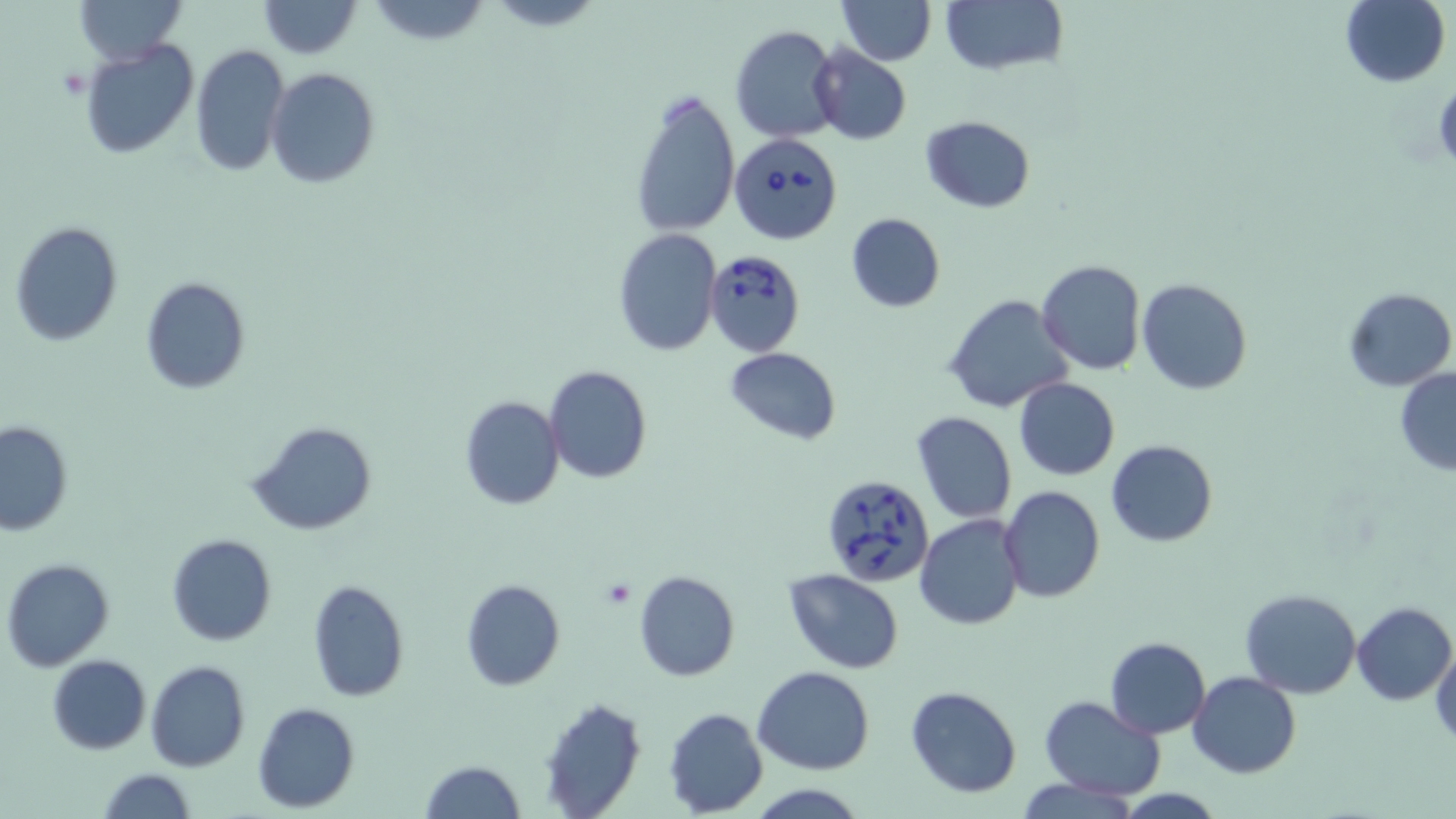 Approximate bounding boxes as named x1/y1/x2/y2 corners in pixels. Babesia divergens-infected red blood cell locations: (x1=731, y1=131, x2=844, y2=244), (x1=702, y1=246, x2=807, y2=355), (x1=820, y1=473, x2=934, y2=585). Uninfected red blood cell locations: (x1=77, y1=0, x2=185, y2=66), (x1=257, y1=0, x2=362, y2=58), (x1=484, y1=0, x2=606, y2=31), (x1=836, y1=0, x2=935, y2=65), (x1=940, y1=0, x2=1068, y2=77), (x1=1341, y1=0, x2=1450, y2=87), (x1=367, y1=1, x2=493, y2=48), (x1=731, y1=25, x2=842, y2=143), (x1=80, y1=39, x2=199, y2=158), (x1=191, y1=42, x2=289, y2=176), (x1=809, y1=43, x2=912, y2=145), (x1=265, y1=68, x2=379, y2=188), (x1=628, y1=86, x2=741, y2=239), (x1=919, y1=115, x2=1035, y2=213), (x1=846, y1=211, x2=945, y2=311), (x1=10, y1=221, x2=123, y2=347), (x1=613, y1=229, x2=721, y2=356), (x1=1036, y1=259, x2=1147, y2=375), (x1=140, y1=277, x2=251, y2=393), (x1=1136, y1=277, x2=1252, y2=395), (x1=1343, y1=287, x2=1455, y2=392), (x1=942, y1=293, x2=1074, y2=415), (x1=724, y1=347, x2=843, y2=443), (x1=543, y1=365, x2=653, y2=484), (x1=1395, y1=368, x2=1456, y2=475), (x1=1014, y1=377, x2=1120, y2=480), (x1=460, y1=395, x2=564, y2=509), (x1=911, y1=410, x2=1018, y2=525), (x1=0, y1=420, x2=73, y2=536), (x1=246, y1=421, x2=378, y2=536), (x1=1105, y1=440, x2=1217, y2=547), (x1=848, y1=482, x2=1004, y2=603), (x1=999, y1=485, x2=1105, y2=602), (x1=915, y1=514, x2=1025, y2=629), (x1=167, y1=533, x2=277, y2=646), (x1=2, y1=559, x2=116, y2=673), (x1=784, y1=568, x2=905, y2=673), (x1=634, y1=570, x2=739, y2=681), (x1=461, y1=577, x2=565, y2=691), (x1=306, y1=579, x2=409, y2=702), (x1=1241, y1=587, x2=1362, y2=698), (x1=1352, y1=601, x2=1455, y2=705), (x1=1105, y1=636, x2=1211, y2=738), (x1=1429, y1=646, x2=1456, y2=746), (x1=48, y1=654, x2=151, y2=754), (x1=145, y1=660, x2=251, y2=772), (x1=753, y1=666, x2=876, y2=775), (x1=1190, y1=672, x2=1300, y2=777), (x1=905, y1=684, x2=1022, y2=798), (x1=537, y1=695, x2=646, y2=818), (x1=1040, y1=695, x2=1166, y2=800), (x1=251, y1=702, x2=361, y2=812), (x1=664, y1=707, x2=767, y2=816), (x1=421, y1=760, x2=525, y2=818), (x1=97, y1=768, x2=197, y2=819), (x1=1015, y1=776, x2=1144, y2=818), (x1=747, y1=784, x2=867, y2=817). Platelet locations: (x1=601, y1=577, x2=638, y2=610). Slide-level diagnosis: Babesia divergens. Image is 1456×819 pixels. Thin blood film. May-Grünwald-Giemsa stain. One field of a larger specimen. 1000x magnification. Optical microscopy.